Assess this cell for malaria.
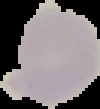

It is uninfected.

From a thin blood film. Image is 100×109 pixels. Segmented cell region on a black background.